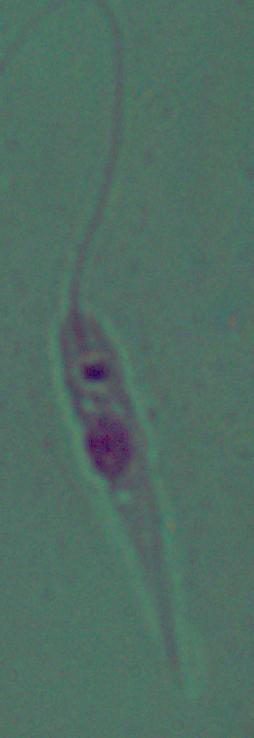

identification = Leishmania
modality = micrograph
magnification = 1000x